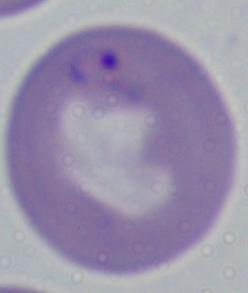

modality: micrograph
magnification: 1000x
identification: Babesia